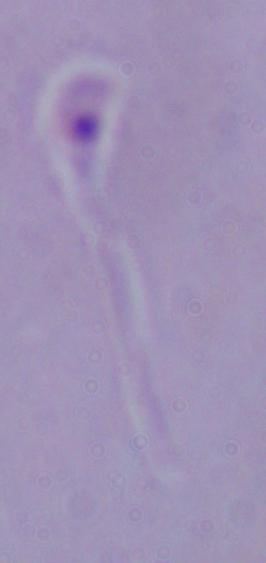
identification = Leishmania
magnification = 1000x
modality = photomicrograph